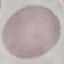 Result: no malaria parasites detected. Automatically extracted cell patch, resized to 64 × 64 pixels. Acquired by smartphone through the microscope eyepiece. Giemsa-stained preparation. Thin blood film.